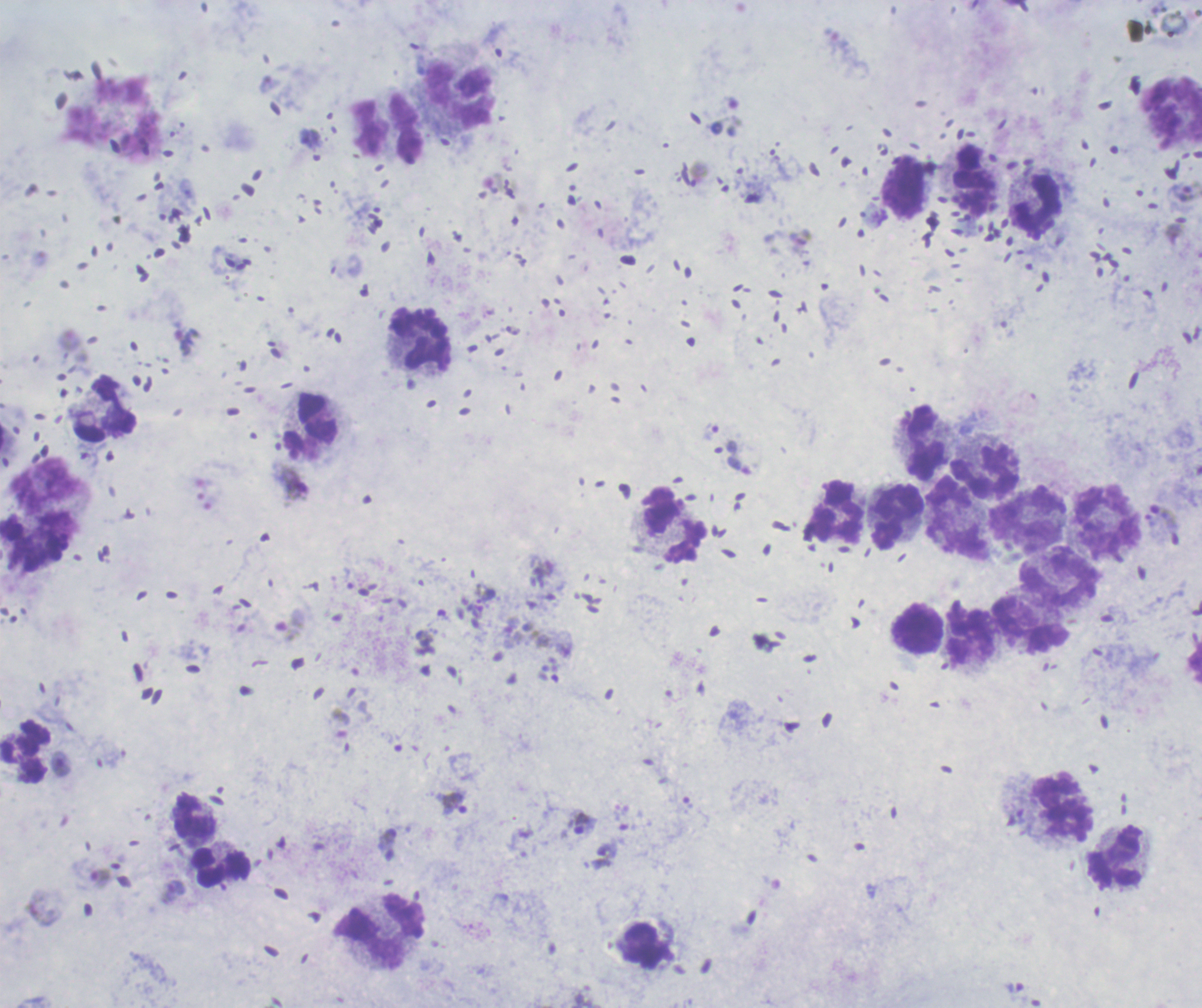

life_cycle_stages_observed: trophozoite, gametocyte
image_size: 1202×1008 pixels
trophozoite_locations: 'approximate centers as [x, y] in pixels: [1185, 190], [455, 802], [582, 823], [101, 878]'
result: Plasmodium parasites identified
field_of_view: one from this slide
preparation: thick blood film
magnification: 100x
context: previously used in an actual diagnosis
stain: Romanowsky
gametocyte_locations: 'approximate centers as [x, y] in pixels: [294, 482], [290, 624], [174, 891]'
leukocyte_locations: 'approximate centers as [x, y] in pixels: [460, 95], [389, 129], [974, 179], [905, 189], [1037, 205], [422, 339], [106, 409], [310, 426], [925, 442], [985, 473], [46, 487], [836, 511], [897, 517], [959, 519], [1108, 519], [1028, 520], [672, 527], [1061, 579], [1031, 626], [918, 629], [970, 632], [25, 752], [1063, 807], [194, 816], [1117, 857], [221, 867], [380, 933]'
background_quality: satisfactory